Classify this cell by malaria status.
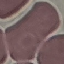

It is uninfected.

stain = Giemsa
image type = cell patch, automatically extracted from a larger field of view and resized to 64 × 64 pixels
preparation = thin blood smear
capture = smartphone through the microscope eyepiece